Point out each leukocyte.
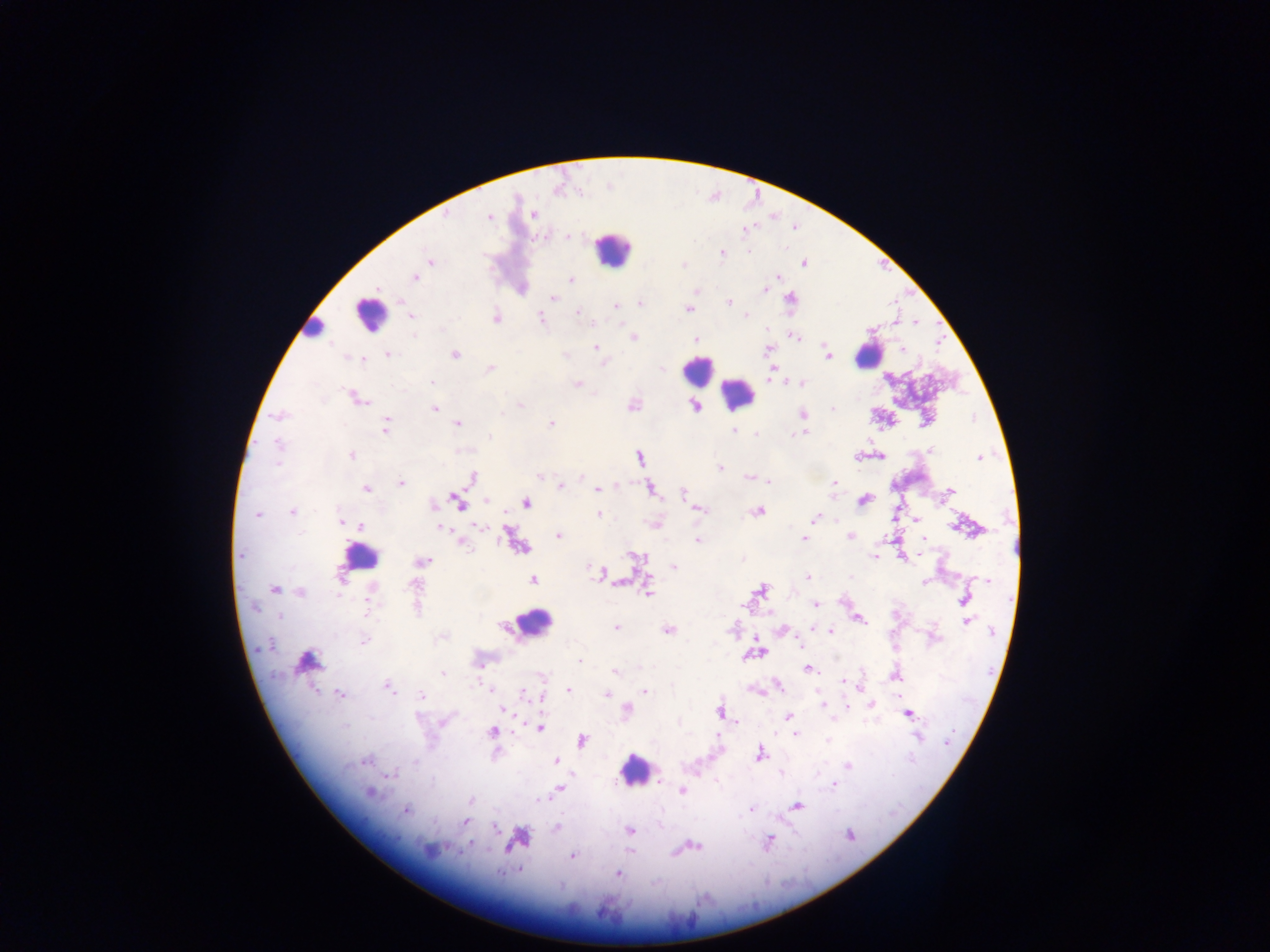
Approximate centers as {x, y} in pixels.
Leukocytes: {612, 249}, {369, 313}, {312, 328}, {867, 356}, {698, 371}, {738, 393}, {360, 556}, {532, 623}, {635, 770}.

Summary:
  - Plasmodium parasite locations: {534, 214}, {488, 216}, {744, 229}, {568, 236}, {749, 252}, {722, 254}, {429, 261}, {804, 263}, {684, 265}, {778, 276}, {414, 278}, {571, 279}, {764, 290}, {696, 291}, {553, 297}, {791, 298}, {728, 302}, {640, 303}, {615, 306}, {688, 309}, {578, 312}, {411, 315}, {746, 316}, {495, 318}, {541, 319}, {415, 335}, {794, 336}, {633, 338}, {696, 339}, {596, 347}, {902, 350}, {767, 351}, {388, 354}, {828, 354}, {455, 355}, {565, 355}, {360, 359}, {601, 359}, {490, 368}, {772, 380}, {431, 382}, {802, 382}, {577, 383}, {357, 399}, {634, 404}, {521, 405}, {694, 406}, {434, 409}, {833, 409}, {501, 413}, {804, 414}, {279, 415}, {458, 423}, {551, 424}, {385, 426}, {734, 431}, {795, 433}, {804, 433}, {758, 434}, {491, 436}, {278, 444}, {930, 451}, {352, 456}, {882, 456}, {639, 457}, {857, 457}, {979, 458}, {278, 462}, {720, 468}, {539, 476}, {473, 477}, {580, 477}, {749, 477}, {768, 481}, {835, 482}, {401, 483}, {617, 483}, {560, 486}, {598, 488}, {650, 488}, {366, 489}, {950, 491}, {684, 493}, {486, 500}, {863, 501}, {457, 502}, {527, 503}, {433, 506}, {698, 509}, {292, 511}, {758, 511}, {257, 514}, {599, 514}, {815, 518}, {917, 519}, {341, 522}, {361, 526}, {478, 526}, {442, 527}, {301, 533}, {559, 536}, {850, 536}, {804, 538}, {923, 538}, {514, 539}, {698, 541}, {463, 543}, {919, 554}, {241, 555}, {874, 557}, {637, 558}, {422, 562}, {674, 567}, {591, 568}, {595, 573}, {341, 576}, {852, 576}, {807, 577}, {533, 580}, {987, 580}, {923, 582}, {413, 585}, {275, 588}, {648, 591}, {760, 591}, {300, 592}, {338, 595}, {964, 598}, {815, 604}, {254, 608}, {368, 609}, {965, 610}, {280, 616}, {859, 619}, {967, 621}, {617, 627}, {668, 630}, {782, 631}, {992, 631}, {830, 632}, {442, 637}, {934, 638}, {363, 641}, {800, 644}, {268, 646}, {756, 653}, {307, 660}, {580, 661}, {478, 663}, {641, 666}, {808, 669}, {615, 672}, {443, 673}, {896, 675}, {543, 677}, {844, 680}, {387, 687}, {778, 687}, {490, 689}, {568, 690}, {644, 691}, {340, 694}, {524, 694}, {607, 694}, {421, 696}, {822, 704}, {871, 705}, {846, 707}, {627, 709}, {506, 710}, {719, 711}, {909, 713}, {790, 716}, {419, 717}, {449, 718}, {445, 721}, {678, 722}, {539, 728}, {493, 731}, {796, 734}, {918, 736}, {827, 740}, {582, 741}, {759, 754}, {366, 760}, {556, 761}, {847, 765}, {392, 774}, {781, 774}, {833, 784}, {559, 788}, {682, 791}, {370, 793}, {539, 800}, {470, 801}, {797, 806}, {750, 809}, {406, 810}, {465, 822}, {495, 827}, {557, 828}, {630, 831}, {848, 834}, {519, 838}, {769, 842}, {472, 845}, {692, 846}, {429, 850}, {630, 851}, {676, 851}, {572, 856}, {500, 873}, {618, 874}
  - Field of view: single
  - Image size: 1270×952 pixels
  - Country: Ghana
  - Capture: mobile-phone photograph through a microscope
  - Preparation: thick blood film